Identify the parasite.
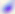
Toxoplasma gondii.

{
  "modality": "photomicrograph",
  "magnification": "400x"
}